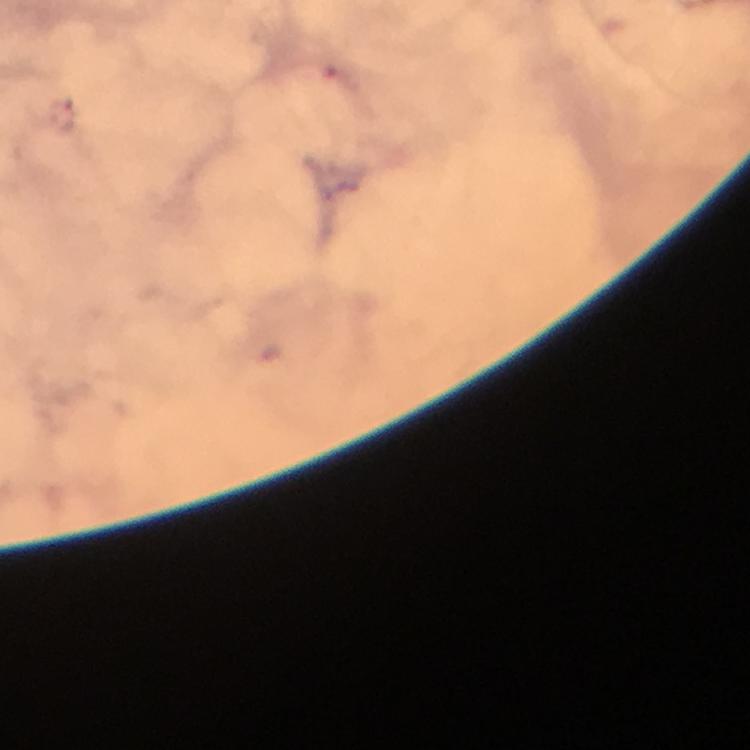

Approximate object centers, in pixels from the top-left corner.
Summary:
  - Plasmodium parasite locations: (x=64, y=114)
  - Cropped from: a single field of view
  - Image size: 750×750 pixels
  - Preparation: thick blood smear
  - Stain: Giemsa
  - Capture: smartphone photograph through a microscope
  - Context: from a diagnostic examination for malaria
  - Magnification: 100x
  - Immersion oil: used